Locate every Plasmodium parasite.
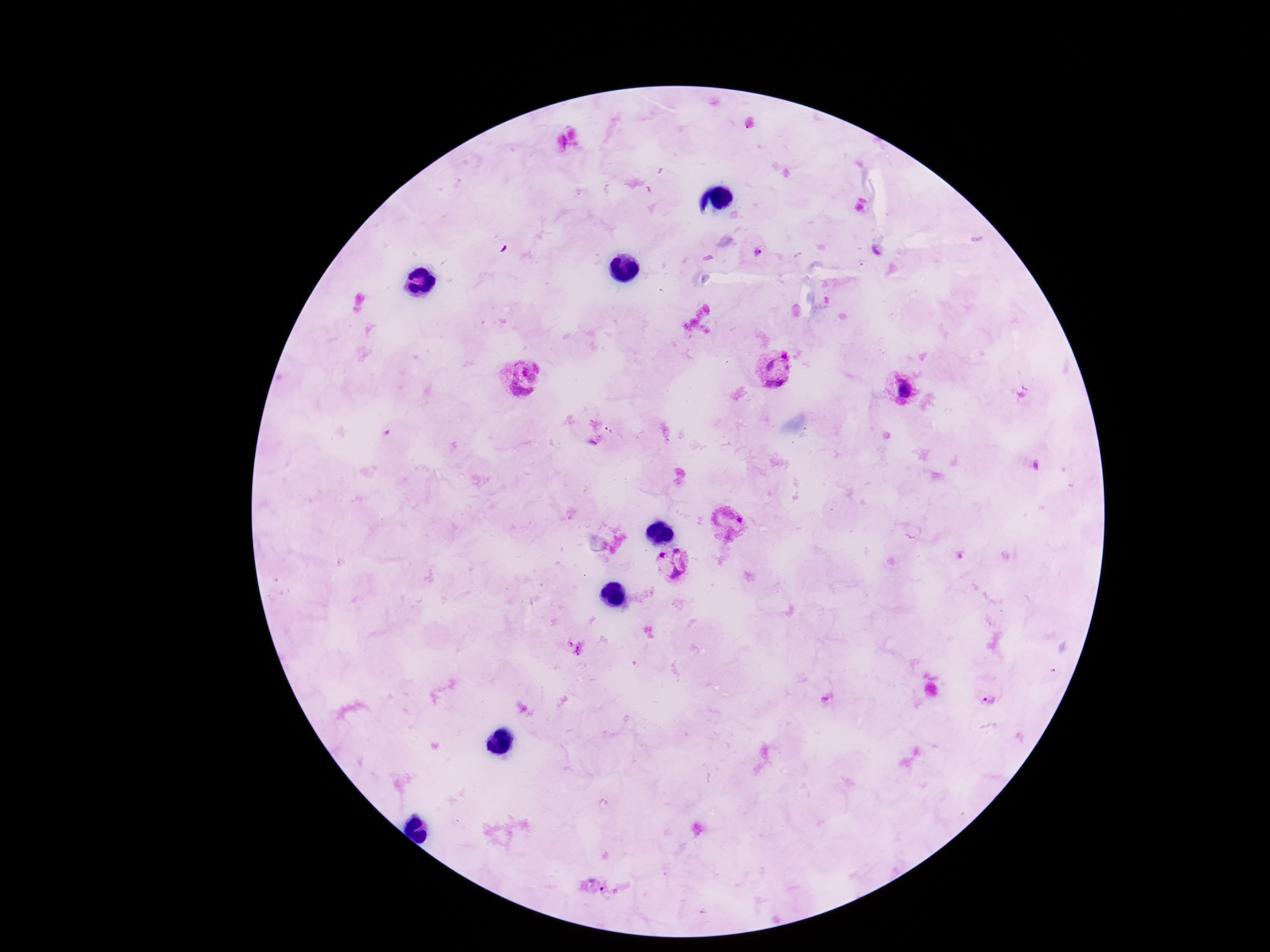
Approximate centers as (x, y) in pixels.
Plasmodium parasites: (759, 252), (775, 367), (522, 379), (903, 388), (1021, 392), (730, 518), (677, 564), (575, 648), (990, 698).

Smartphone photograph taken through the microscope eyepiece. 100x magnification. Patient malaria status: infected. Thick blood smear. Giemsa-stained preparation. One field from this slide. Image is 1270×952 pixels.